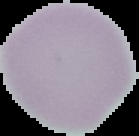

image type = segmented cell region on a black background
malaria status = uninfected
preparation = thin blood film
image size = 139×136 pixels